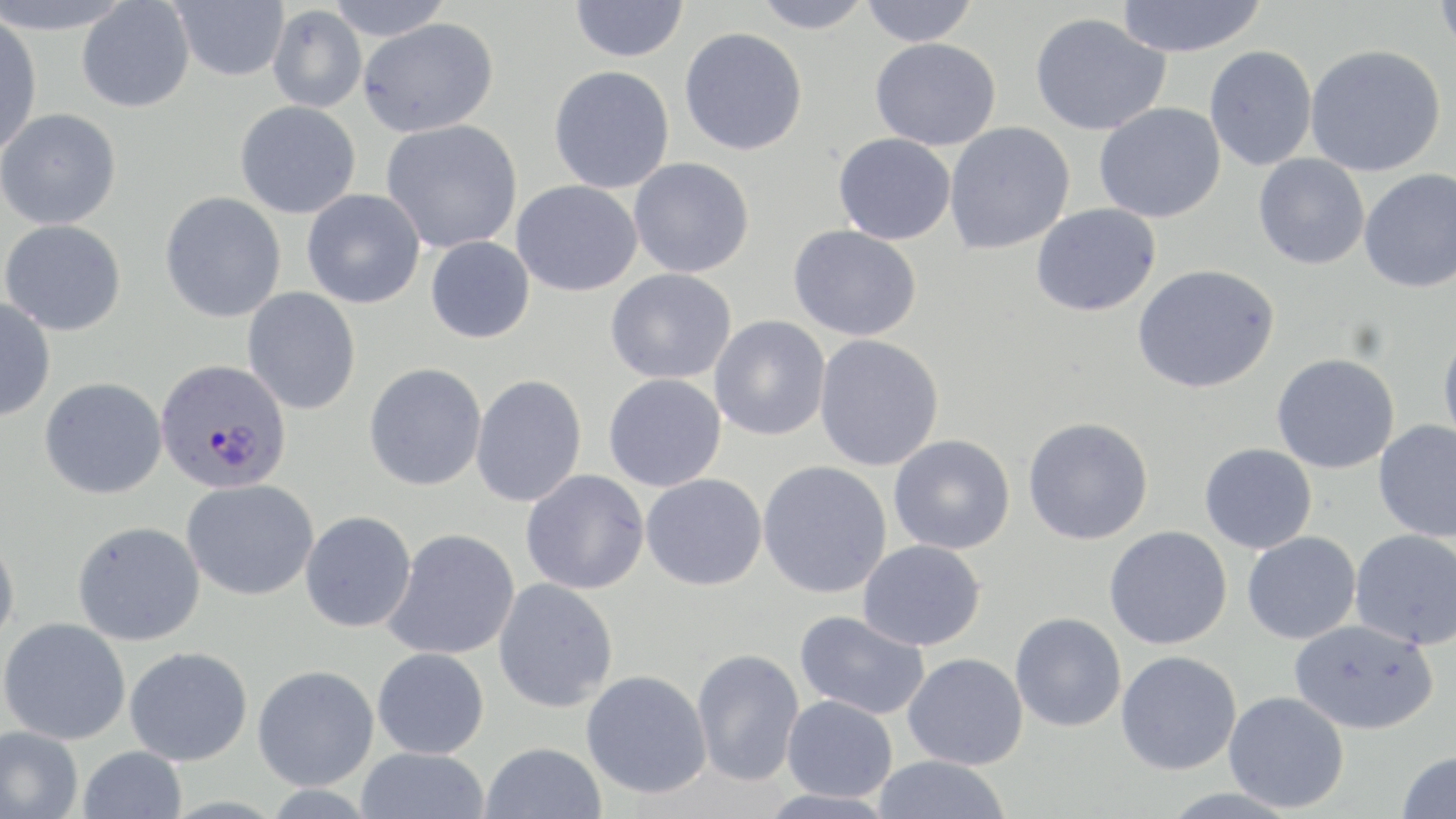

slide_level_diagnosis: Plasmodium falciparum
image_size: 1456×819 pixels
stain: May-Grünwald-Giemsa
modality: optical microscopy
uninfected_red_blood_cell_locations: 'approximate bounding boxes as named x1/y1/x2/y2 corners in pixels: (x1=0, y1=0, x2=135, y2=34), (x1=325, y1=0, x2=453, y2=41), (x1=570, y1=0, x2=689, y2=62), (x1=750, y1=0, x2=874, y2=33), (x1=1116, y1=0, x2=1268, y2=57), (x1=1434, y1=0, x2=1456, y2=57), (x1=76, y1=1, x2=195, y2=113), (x1=170, y1=1, x2=289, y2=81), (x1=860, y1=1, x2=978, y2=46), (x1=267, y1=6, x2=367, y2=112), (x1=1029, y1=12, x2=1169, y2=136), (x1=0, y1=16, x2=42, y2=155), (x1=357, y1=18, x2=499, y2=138), (x1=679, y1=28, x2=808, y2=156), (x1=870, y1=38, x2=1001, y2=150), (x1=1305, y1=44, x2=1446, y2=177), (x1=1204, y1=45, x2=1317, y2=171), (x1=548, y1=65, x2=675, y2=194), (x1=234, y1=100, x2=361, y2=219), (x1=1093, y1=103, x2=1225, y2=223), (x1=0, y1=108, x2=121, y2=230), (x1=380, y1=120, x2=522, y2=254), (x1=944, y1=122, x2=1074, y2=254), (x1=833, y1=133, x2=956, y2=245), (x1=1253, y1=154, x2=1369, y2=269), (x1=628, y1=157, x2=754, y2=278), (x1=1359, y1=169, x2=1456, y2=294), (x1=511, y1=180, x2=642, y2=297), (x1=301, y1=189, x2=425, y2=309), (x1=159, y1=192, x2=286, y2=323), (x1=1030, y1=203, x2=1161, y2=317), (x1=0, y1=219, x2=126, y2=336), (x1=787, y1=225, x2=921, y2=341), (x1=425, y1=236, x2=534, y2=344), (x1=1132, y1=265, x2=1279, y2=393), (x1=605, y1=269, x2=736, y2=384), (x1=242, y1=287, x2=361, y2=415), (x1=0, y1=298, x2=55, y2=422), (x1=709, y1=315, x2=830, y2=442), (x1=1438, y1=329, x2=1456, y2=449), (x1=814, y1=334, x2=944, y2=472), (x1=1271, y1=353, x2=1400, y2=474), (x1=363, y1=363, x2=487, y2=491), (x1=470, y1=374, x2=587, y2=508), (x1=603, y1=374, x2=726, y2=492), (x1=39, y1=377, x2=167, y2=499), (x1=1022, y1=417, x2=1153, y2=546), (x1=1373, y1=421, x2=1456, y2=542), (x1=888, y1=434, x2=1015, y2=554), (x1=1199, y1=443, x2=1317, y2=554), (x1=756, y1=461, x2=892, y2=598), (x1=520, y1=469, x2=649, y2=595), (x1=640, y1=473, x2=767, y2=591), (x1=181, y1=479, x2=319, y2=601), (x1=299, y1=511, x2=417, y2=633), (x1=72, y1=521, x2=205, y2=646), (x1=1104, y1=526, x2=1232, y2=649), (x1=383, y1=529, x2=520, y2=661), (x1=1350, y1=529, x2=1456, y2=650), (x1=1242, y1=531, x2=1361, y2=644), (x1=0, y1=532, x2=20, y2=648), (x1=857, y1=540, x2=985, y2=651), (x1=492, y1=578, x2=618, y2=713), (x1=794, y1=610, x2=930, y2=721), (x1=1009, y1=612, x2=1126, y2=732), (x1=0, y1=618, x2=130, y2=744), (x1=1288, y1=619, x2=1439, y2=734), (x1=124, y1=647, x2=253, y2=766), (x1=372, y1=647, x2=489, y2=759), (x1=691, y1=648, x2=804, y2=787), (x1=1115, y1=650, x2=1241, y2=775), (x1=903, y1=653, x2=1027, y2=770), (x1=252, y1=664, x2=379, y2=790), (x1=581, y1=670, x2=711, y2=799), (x1=1223, y1=690, x2=1350, y2=813), (x1=783, y1=695, x2=897, y2=803), (x1=1, y1=725, x2=83, y2=819), (x1=480, y1=742, x2=607, y2=819), (x1=78, y1=746, x2=187, y2=819), (x1=356, y1=747, x2=490, y2=819), (x1=1396, y1=749, x2=1456, y2=819), (x1=872, y1=755, x2=1012, y2=819)'
preparation: thin blood film
magnification: 1000x
plasmodium_falciparum_infected_red_blood_cell_locations: 'approximate bounding boxes as named x1/y1/x2/y2 corners in pixels: (x1=155, y1=358, x2=292, y2=494)'
field_of_view: single